State which parasite is depicted.
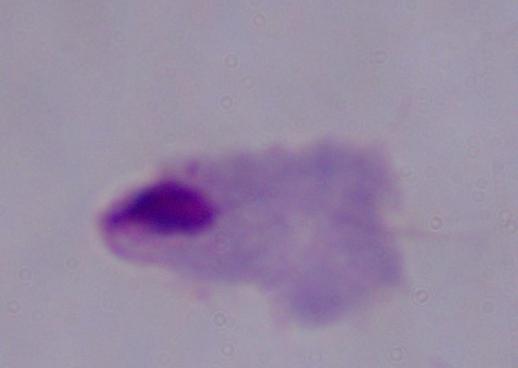
A trichomonad.

Micrograph. 1000x magnification.